Locate platelets.
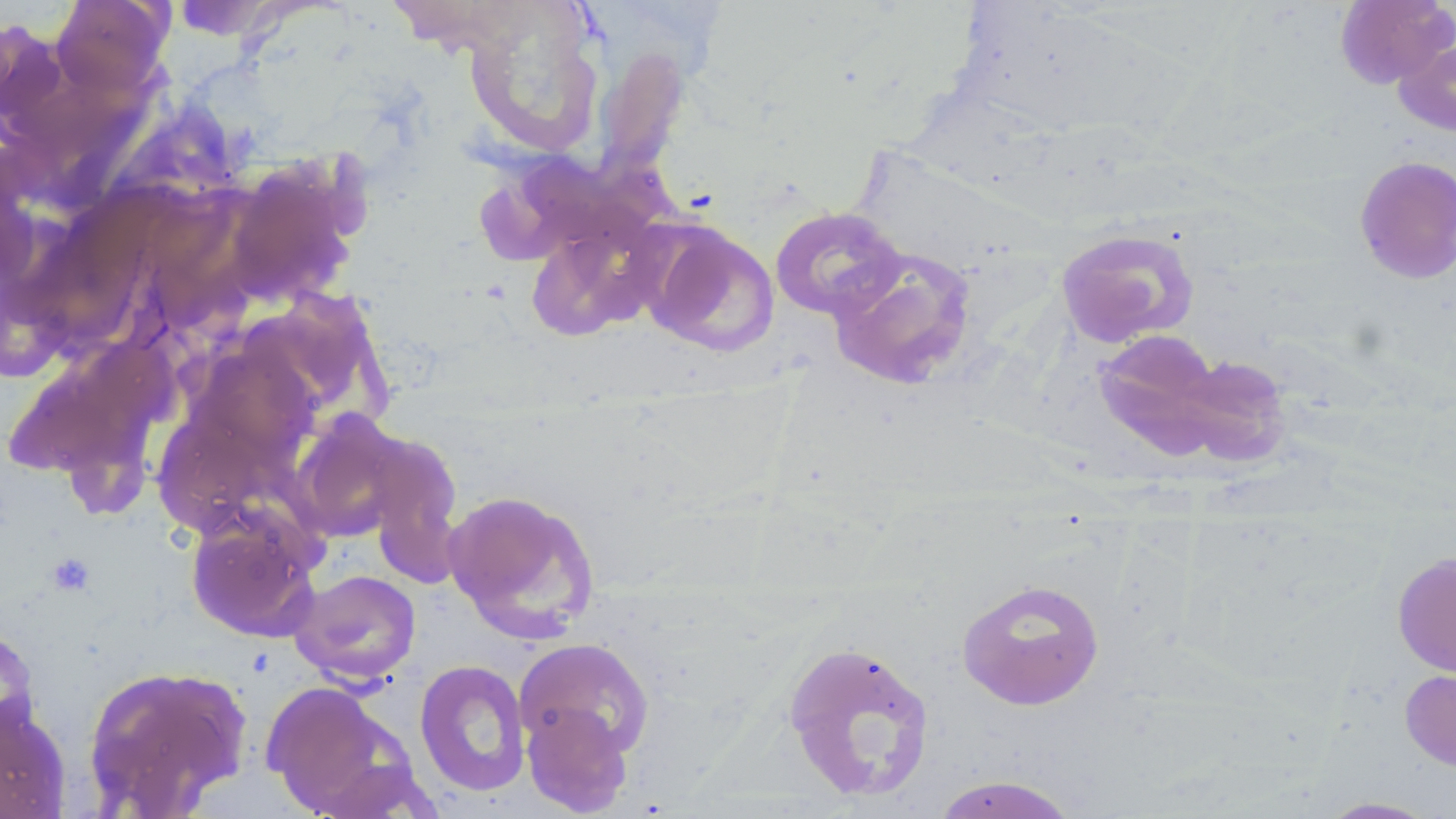

Approximate bounding boxes as (x1, y1, x2, y2) in pixels.
Platelets: (45, 551, 96, 596).

Summary:
  - Uninfected red blood cell locations: (49, 0, 174, 98), (386, 0, 531, 53), (1334, 0, 1455, 89), (461, 5, 604, 159), (1393, 34, 1456, 138), (592, 48, 689, 187), (1353, 154, 1456, 285), (769, 206, 906, 320), (525, 217, 660, 342), (644, 221, 779, 358), (1056, 227, 1199, 349), (827, 247, 979, 390), (1084, 329, 1285, 479), (0, 341, 163, 490), (291, 412, 412, 541), (362, 429, 465, 590), (442, 487, 601, 641), (186, 512, 323, 643), (1392, 551, 1456, 678), (289, 569, 421, 685), (956, 577, 1105, 711), (0, 624, 41, 746), (513, 638, 655, 764), (780, 638, 936, 803), (414, 659, 532, 797), (81, 662, 254, 818), (1400, 667, 1456, 773), (261, 682, 418, 817), (0, 695, 71, 819), (521, 700, 634, 816), (929, 775, 1080, 818), (1316, 796, 1442, 818)
  - Slide-level diagnosis: negative for blood parasites
  - Stain: May-Grünwald-Giemsa
  - Field of view: one of a larger specimen
  - Image size: 1456×819 pixels
  - Modality: light microscopy
  - Magnification: 1000x
  - Preparation: thin blood smear